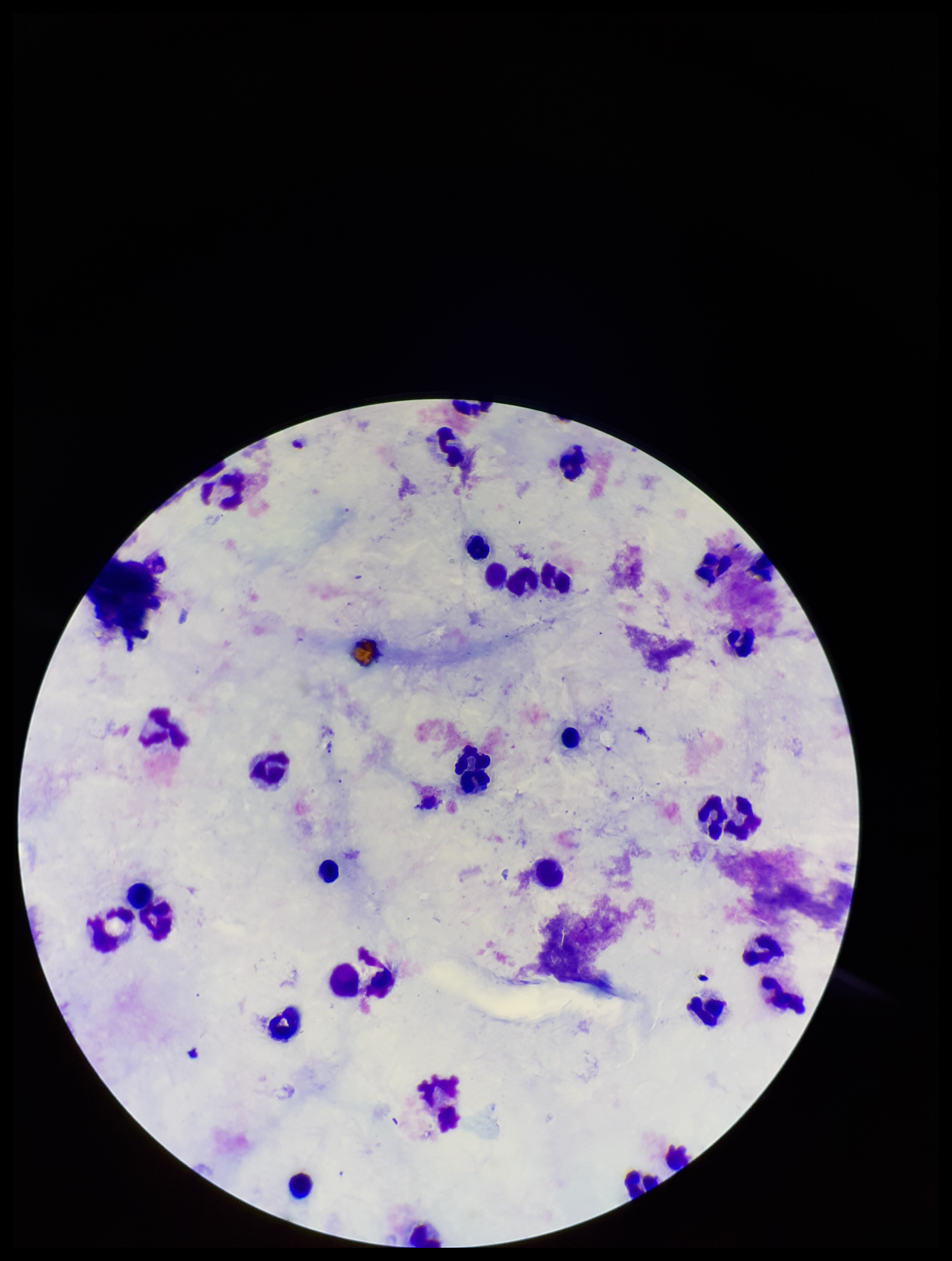

Plasmodium parasites: none detected. Leukocyte count: 31. Preparation: thick blood smear. Parasite count: 0. Patient malaria status: negative. One field from this slide. Image is 952×1261 pixels. Smartphone photograph taken through the eyepiece of a microscope. Stained with Giemsa.